Comment on the morphology of the erythrocytes.
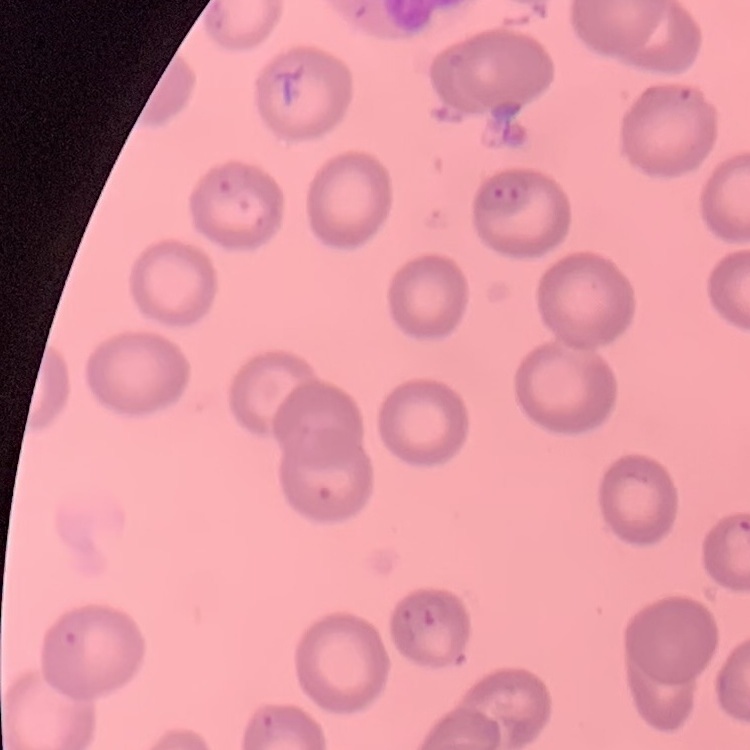
No rouleaux formation.

Stained with either Field's or Giemsa. One tile cut from a larger photomicrograph. Thin peripheral smear.